Identify the parasite.
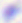

This is Toxoplasma gondii.

modality = photomicrograph
magnification = 400x